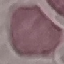

{
  "malaria_status": "uninfected",
  "image_type": "automatically extracted cell patch, resized to 64 × 64 pixels",
  "stain": "Giemsa",
  "capture": "smartphone through the microscope eyepiece",
  "preparation": "thin blood film"
}